Identify the parasite.
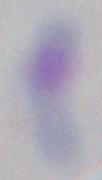

Toxoplasma gondii.

Micrograph. Captured at 1000x magnification.